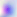

Captured at 400x magnification. Photomicrograph. Toxoplasma gondii is seen.